Locate every Plasmodium ovale-infected red blood cell.
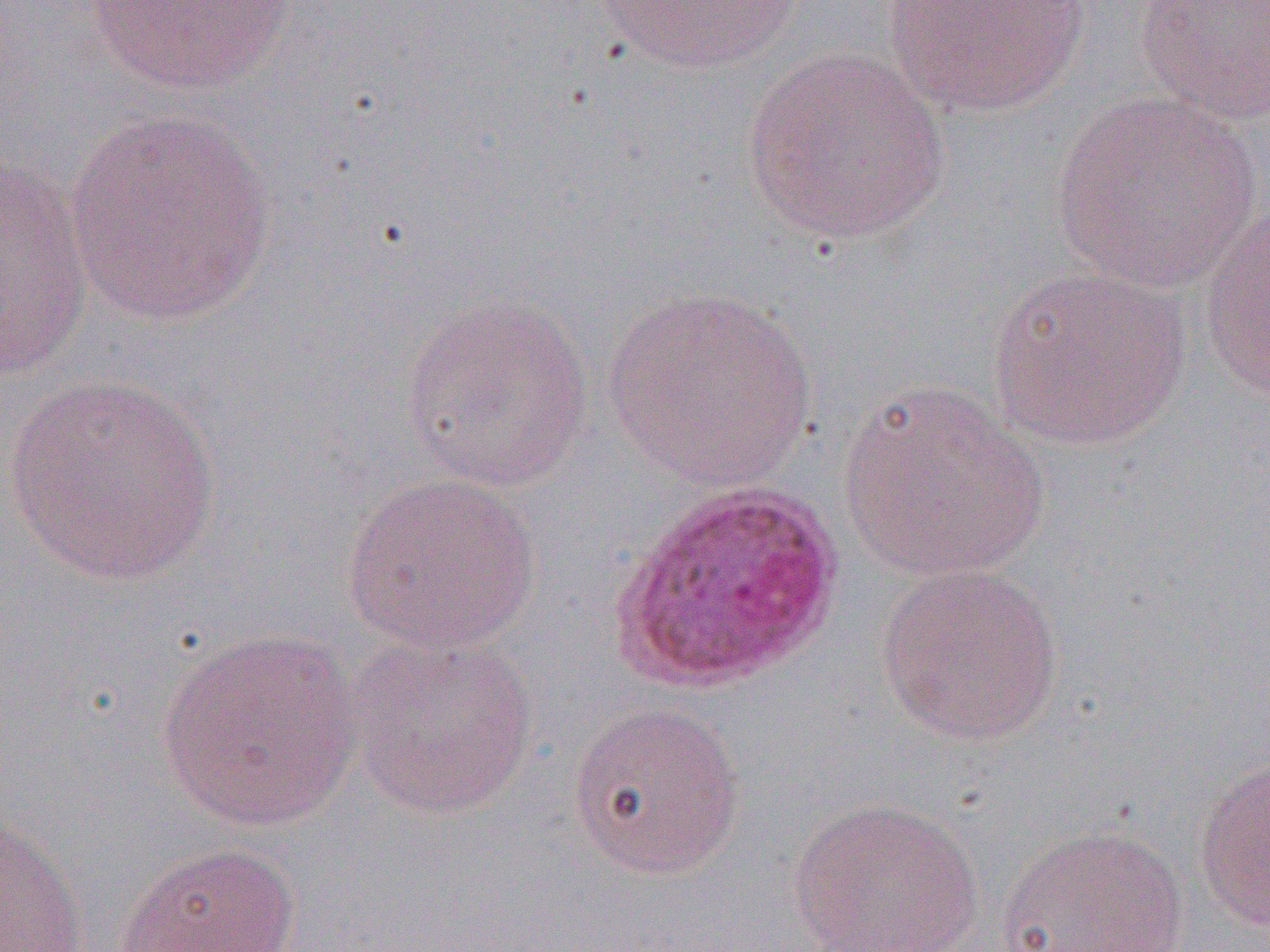

Approximate bounding boxes as (x1,y1)-(x2,y2) corner pairs in pixels.
Plasmodium ovale-infected red blood cells: (609,478)-(843,694).

slide_level_diagnosis: Plasmodium ovale
preparation: thin blood film
modality: light microscopy
image_size: 1270×952 pixels
magnification: 1000x
field_of_view: one of a larger specimen
uninfected_red_blood_cell_locations: 'approximate bounding boxes as (x1,y1)-(x2,y2) corner pairs in pixels: (587,0)-(810,75), (881,0)-(1092,118), (1135,0)-(1270,126), (81,1)-(294,95), (740,49)-(953,247), (1048,92)-(1266,292), (60,110)-(279,328), (1,158)-(94,382), (1198,208)-(1270,404), (984,265)-(1191,453), (600,287)-(821,491), (400,295)-(595,492), (1,374)-(224,588), (835,380)-(1053,586), (340,472)-(541,655), (876,562)-(1065,748), (153,627)-(367,833), (342,631)-(541,821), (566,700)-(746,881), (1194,756)-(1270,934), (785,796)-(985,951), (0,812)-(91,952), (994,824)-(1190,952), (112,842)-(302,951)'